Locate and identify every blood parasite.
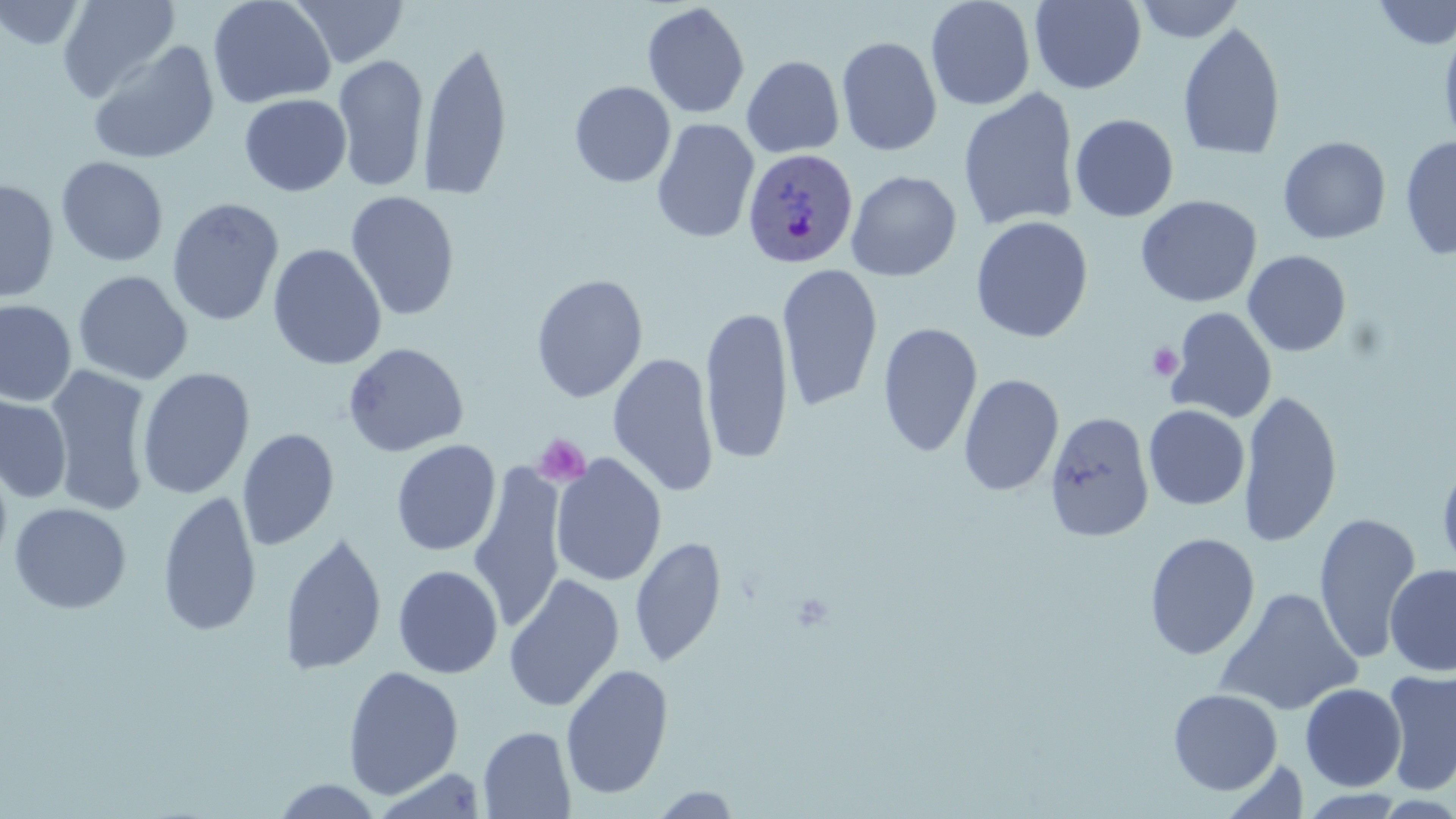
Approximate bounding boxes as (x1,y1)-(x2,y2) corner pairs in pixels.
Plasmodium ovale-infected red blood cells: (742,148)-(857,270).
No Plasmodium falciparum, Plasmodium malariae, Plasmodium vivax, Babesia divergens, or Trypanosoma brucei observed.

Summary:
  - Platelet locations: (1147,343)-(1183,382), (534,434)-(591,487)
  - Uninfected red blood cell locations: (55,0)-(180,103), (208,0)-(335,109), (291,0)-(409,69), (925,0)-(1036,111), (1133,0)-(1245,43), (0,1)-(88,51), (1029,1)-(1146,94), (1372,1)-(1456,49), (642,3)-(751,119), (1177,21)-(1286,161), (1439,22)-(1456,152), (836,36)-(942,156), (86,40)-(220,165), (418,40)-(513,201), (333,53)-(429,193), (742,56)-(844,158), (570,81)-(676,188), (958,87)-(1080,233), (239,93)-(352,196), (1070,114)-(1179,222), (651,119)-(759,244), (1400,135)-(1456,261), (1278,136)-(1391,245), (56,156)-(169,267), (846,170)-(962,281), (0,178)-(59,304), (345,191)-(460,321), (1136,195)-(1262,308), (166,197)-(285,327), (970,216)-(1094,343), (267,244)-(386,370), (1242,250)-(1352,357), (777,264)-(883,412), (73,270)-(193,385), (531,273)-(648,403), (0,299)-(77,407), (700,305)-(794,465), (1165,307)-(1277,425), (878,322)-(983,457), (343,342)-(469,457), (607,352)-(720,497), (44,365)-(155,515), (137,367)-(255,500), (958,374)-(1064,497), (1238,388)-(1343,549), (0,392)-(73,504), (1143,405)-(1250,510), (1044,410)-(1154,543), (237,428)-(339,551), (391,439)-(501,557), (1436,450)-(1456,585), (0,453)-(13,574), (550,453)-(667,588), (469,466)-(566,634), (158,490)-(262,637), (9,503)-(132,614), (1313,512)-(1422,666), (279,532)-(387,677), (1143,532)-(1260,660), (630,535)-(727,668), (1384,564)-(1456,676), (393,565)-(503,679), (503,573)-(624,713), (1214,587)-(1362,716), (560,664)-(674,800), (342,665)-(464,799), (1382,668)-(1456,795), (1299,683)-(1407,792), (1167,688)-(1283,796), (478,726)-(576,819), (1221,759)-(1309,816), (270,778)-(385,818), (650,787)-(744,818), (1296,789)-(1410,817)
  - Slide-level diagnosis: Plasmodium ovale
  - Magnification: 1000x
  - Field of view: one of a larger specimen
  - Modality: light microscopy
  - Image size: 1456×819 pixels
  - Preparation: thin blood film
  - Stain: May-Grünwald-Giemsa